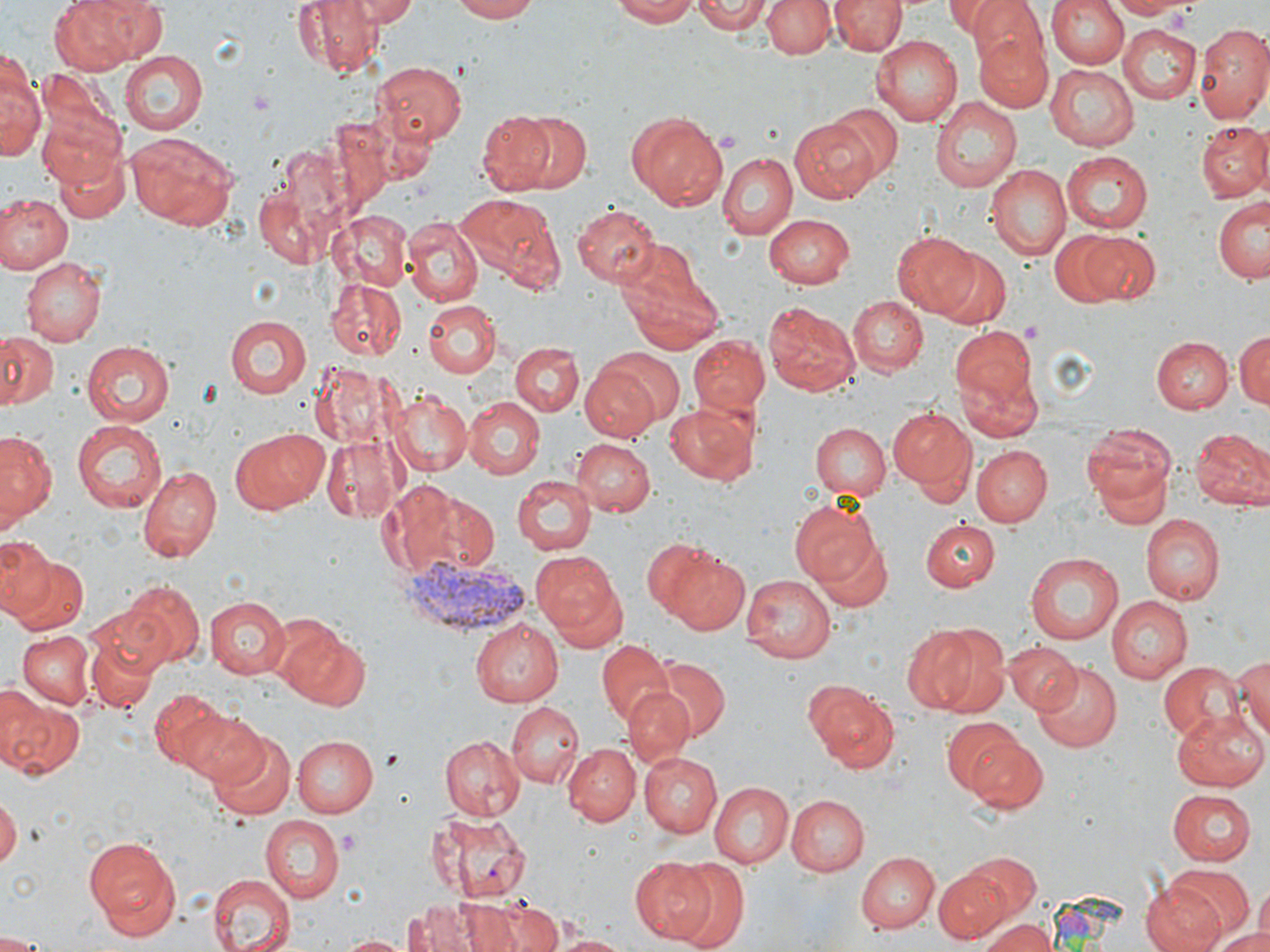 Approximate bounding boxes as (x1, y1, x2, y2) in pixels. Plasmodium vivax-infected red blood cell locations: (402, 559, 533, 636). Uninfected red blood cell locations: (50, 0, 140, 76), (287, 0, 382, 76), (346, 0, 417, 26), (450, 0, 537, 22), (613, 0, 706, 25), (693, 0, 770, 35), (762, 0, 834, 59), (831, 0, 904, 55), (947, 0, 1023, 40), (966, 0, 1049, 74), (1048, 0, 1127, 69), (1110, 0, 1192, 19), (1194, 23, 1270, 124), (1119, 27, 1200, 103), (974, 29, 1055, 112), (869, 35, 963, 126), (2, 51, 43, 163), (120, 51, 208, 136), (371, 60, 467, 144), (1046, 65, 1137, 150), (930, 98, 1021, 193), (826, 101, 902, 181), (37, 106, 130, 192), (483, 107, 587, 198), (626, 111, 728, 210), (789, 117, 878, 203), (1193, 120, 1269, 203), (127, 131, 239, 230), (44, 135, 131, 226), (717, 151, 798, 239), (1060, 151, 1154, 234), (985, 165, 1071, 260), (252, 175, 336, 269), (0, 191, 71, 273), (4, 192, 87, 342), (454, 192, 560, 293), (1213, 195, 1270, 283), (573, 204, 661, 287), (328, 210, 414, 291), (763, 214, 855, 290), (403, 215, 484, 304), (893, 231, 983, 320), (1049, 231, 1121, 307), (1075, 231, 1159, 305), (616, 239, 716, 348), (937, 250, 1012, 329), (19, 256, 107, 343), (326, 277, 406, 361), (848, 296, 928, 377), (423, 300, 498, 377), (763, 302, 860, 397), (223, 314, 311, 397), (949, 326, 1042, 441), (0, 330, 60, 412), (1234, 330, 1270, 411), (688, 335, 771, 416), (1154, 336, 1233, 413), (81, 340, 178, 428), (510, 341, 585, 418), (582, 362, 663, 442), (388, 392, 471, 476), (462, 395, 543, 478), (662, 401, 759, 487), (887, 406, 974, 492), (68, 418, 167, 515), (1082, 422, 1178, 518), (810, 423, 890, 501), (228, 426, 329, 513), (1190, 426, 1269, 510), (0, 429, 57, 532), (319, 432, 406, 522), (569, 437, 655, 516), (972, 445, 1050, 527), (137, 466, 222, 563), (512, 475, 595, 554), (375, 480, 495, 579), (789, 503, 880, 586), (1139, 516, 1223, 605), (921, 518, 998, 591), (812, 534, 893, 612), (0, 536, 55, 617), (653, 543, 751, 635), (12, 552, 89, 636), (532, 552, 625, 639), (1023, 552, 1123, 644), (741, 575, 836, 663), (116, 581, 205, 668), (202, 593, 293, 678), (1105, 597, 1192, 684), (92, 598, 178, 683), (470, 615, 562, 705), (83, 616, 161, 715), (273, 619, 367, 709), (900, 624, 990, 713), (16, 630, 94, 710), (938, 634, 1009, 717), (595, 638, 673, 724), (1004, 641, 1081, 715), (1231, 652, 1270, 748), (647, 654, 729, 741), (1156, 659, 1247, 742), (1032, 662, 1124, 751), (803, 678, 897, 772), (0, 684, 48, 769), (624, 687, 694, 767), (150, 689, 245, 777), (2, 694, 83, 778), (505, 700, 583, 785), (1171, 712, 1268, 792), (184, 714, 269, 791), (941, 718, 1022, 796), (205, 731, 296, 822), (439, 733, 524, 820), (292, 736, 379, 817), (966, 737, 1049, 814), (563, 743, 639, 826), (640, 753, 721, 837), (708, 781, 794, 867), (1167, 789, 1257, 865), (788, 794, 871, 875), (0, 796, 19, 873), (427, 810, 533, 903), (260, 816, 344, 903), (86, 836, 180, 930), (856, 852, 938, 931), (965, 852, 1041, 920), (630, 857, 716, 943), (666, 862, 749, 947), (1168, 865, 1252, 936), (935, 866, 1012, 941), (207, 873, 294, 952), (1140, 882, 1227, 952), (1254, 886, 1269, 938), (457, 895, 538, 952), (494, 898, 564, 952), (407, 901, 479, 952), (980, 916, 1054, 952), (1210, 928, 1270, 952), (0, 932, 50, 952), (549, 933, 635, 951), (340, 934, 410, 952). Slide-level diagnosis: Plasmodium vivax. May-Grünwald-Giemsa-stained preparation. Optical microscopy. One field of a larger specimen. Thin blood smear. Captured at 1000x magnification. Image is 1270×952 pixels.